Assess this cell for malaria.
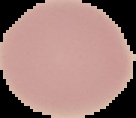

It is uninfected.

Summary:
  - Preparation: thin blood smear
  - Image type: cell region segmented out of the field of view; surrounding area masked to black
  - Image size: 136×118 pixels